Give the preparation type.
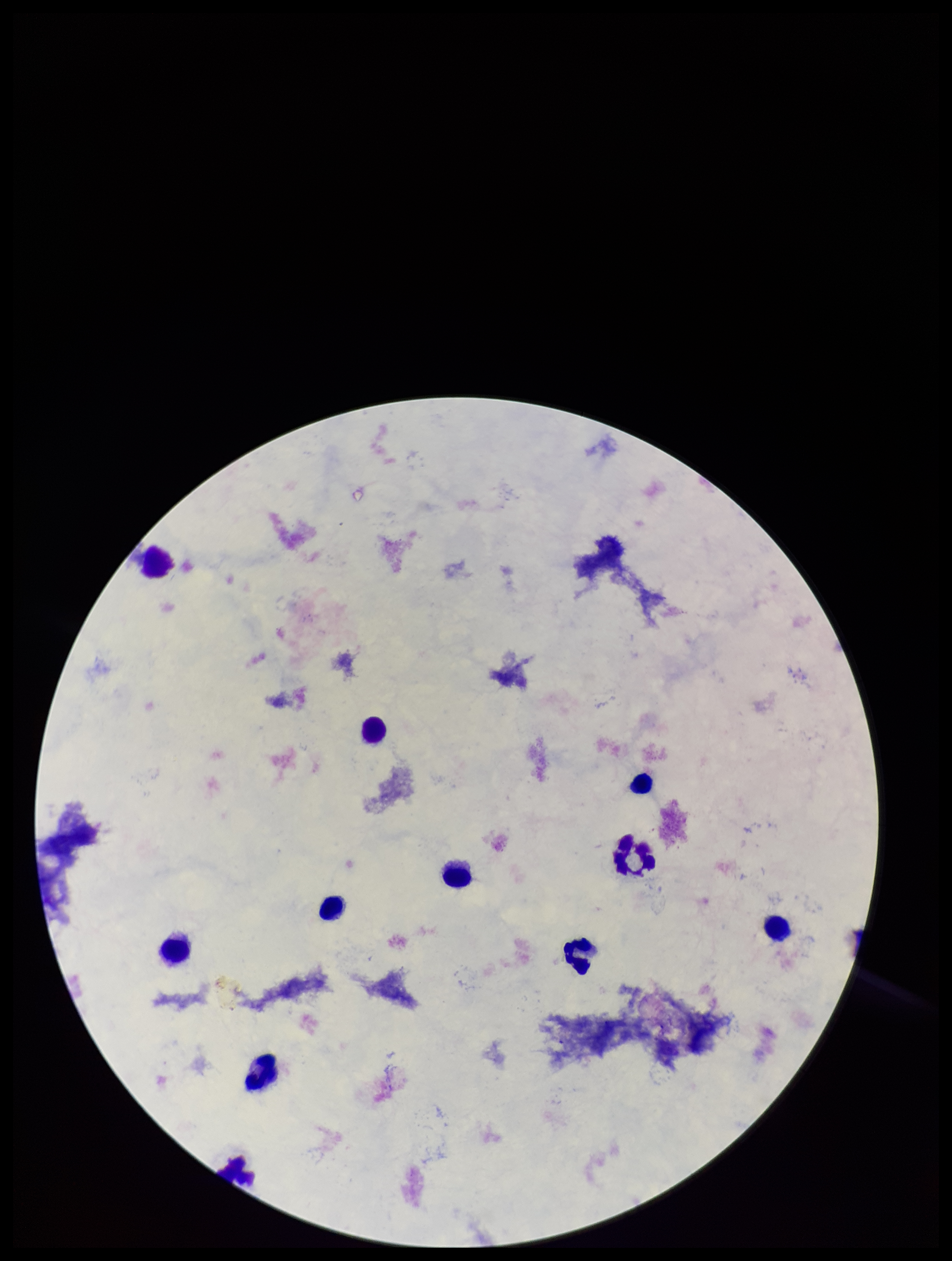

A thick smear.

stain = Giemsa
Plasmodium parasites = none identified
capture = smartphone photograph through the microscope eyepiece
parasite count = 0
leukocyte count = 11
field of view = one from this slide
image size = 952×1261 pixels
patient malaria status = negative